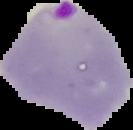
The area outside the segmented cell region is set to black. Image is 133×130 pixels. From a thin blood smear. Result: Plasmodium parasites identified.